Locate every blood parasite and identify its species.
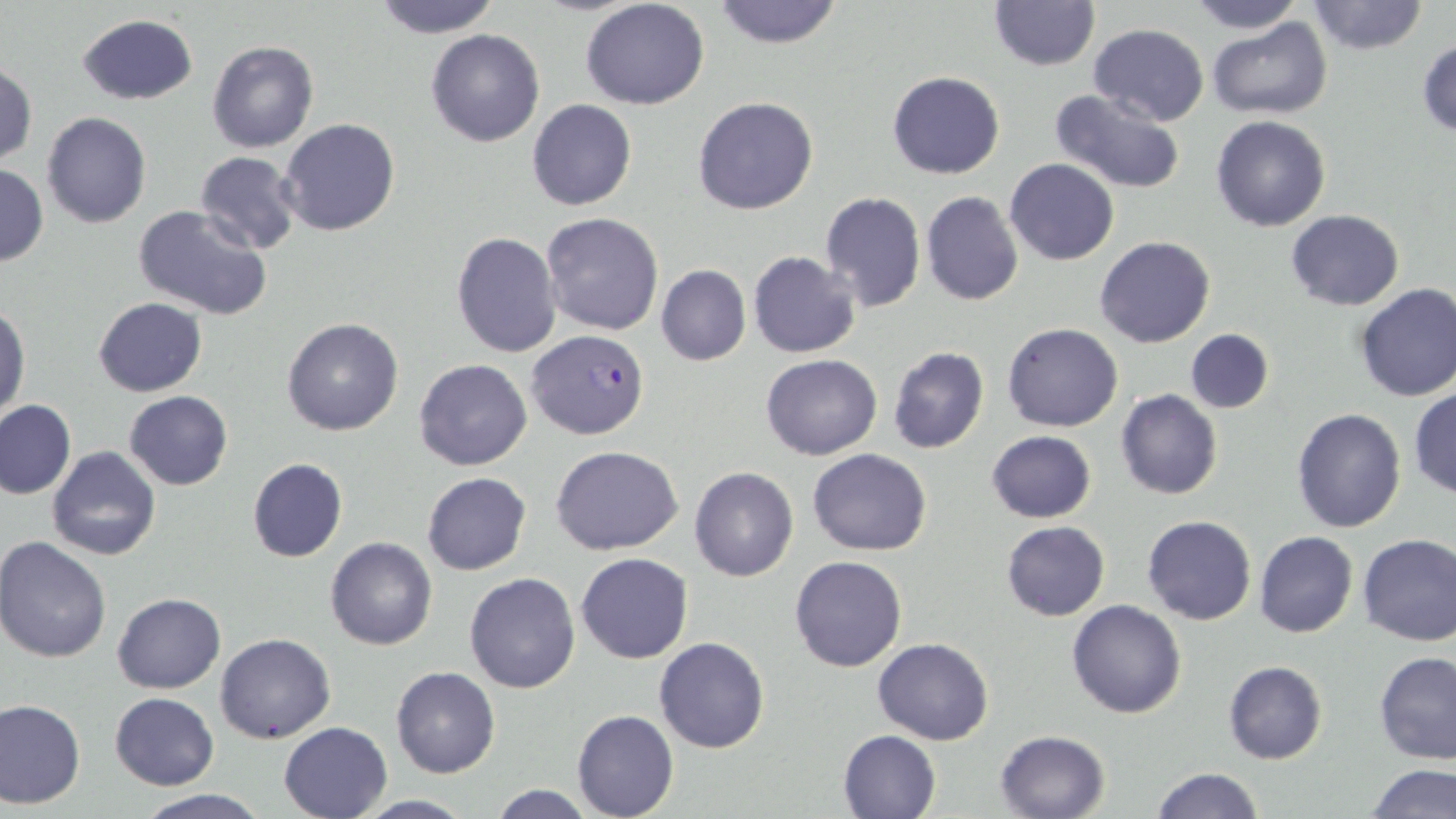
Approximate bounding boxes as (x1,y1)-(x2,y2) corner pairs in pixels.
Plasmodium falciparum-infected red blood cells: (526,328)-(649,442).
No Plasmodium ovale, Plasmodium malariae, Plasmodium vivax, Babesia divergens, or Trypanosoma brucei observed.

Summary:
  - Uninfected red blood cell locations: (371,0)-(504,37), (579,0)-(711,110), (710,0)-(845,49), (1184,0)-(1306,34), (988,1)-(1101,72), (1305,1)-(1430,54), (77,15)-(197,104), (1206,17)-(1332,119), (1088,24)-(1211,126), (426,29)-(545,146), (1416,40)-(1456,140), (206,41)-(318,153), (1,60)-(37,167), (887,71)-(1005,179), (1048,88)-(1189,195), (694,97)-(819,216), (527,99)-(638,209), (42,112)-(151,228), (1210,115)-(1331,231), (280,119)-(400,236), (195,151)-(303,255), (1005,159)-(1118,266), (1,163)-(48,265), (819,191)-(926,314), (920,191)-(1024,307), (133,204)-(273,320), (1285,210)-(1404,309), (540,211)-(666,336), (451,231)-(561,358), (1095,235)-(1216,348), (749,251)-(860,358), (656,265)-(751,366), (1354,282)-(1456,401), (92,298)-(207,397), (1,303)-(29,419), (281,316)-(405,437), (1004,323)-(1124,432), (1186,328)-(1273,414), (887,345)-(989,454), (759,354)-(883,461), (414,358)-(533,470), (1409,386)-(1456,498), (1115,388)-(1224,500), (124,391)-(233,490), (0,399)-(76,499), (1293,407)-(1407,533), (985,430)-(1098,524), (550,445)-(683,555), (47,446)-(161,562), (807,449)-(932,555), (247,458)-(348,561), (689,465)-(800,581), (422,471)-(530,575), (1141,515)-(1256,625), (1002,520)-(1110,620), (1254,531)-(1358,639), (1356,534)-(1456,646), (1,535)-(114,662), (325,536)-(437,650), (576,552)-(693,665), (789,556)-(908,672), (464,572)-(580,693), (112,593)-(225,693), (1065,600)-(1186,719), (215,633)-(337,744), (654,637)-(771,754), (872,638)-(995,745), (1374,651)-(1456,764), (1223,661)-(1327,765), (391,667)-(499,778), (109,692)-(219,789), (0,697)-(86,808), (572,708)-(679,819), (278,721)-(394,818), (839,729)-(942,818), (995,730)-(1111,818), (1364,764)-(1454,817), (1149,767)-(1264,819), (487,783)-(598,819), (133,789)-(271,819), (355,795)-(479,817)
  - Slide-level diagnosis: Plasmodium falciparum
  - Image size: 1456×819 pixels
  - Modality: light microscopy
  - Preparation: thin blood smear
  - Stain: May-Grünwald-Giemsa
  - Field of view: one of a larger specimen
  - Magnification: 1000x